Assess this cell for malaria.
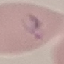

Parasitized.

Summary:
  - Stain: Giemsa
  - Image type: cell patch, automatically extracted from a larger field of view and resized to 64 × 64 pixels
  - Capture: smartphone camera at the microscope eyepiece
  - Preparation: thin smear